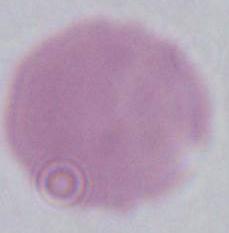
magnification = 1000x
modality = micrograph
identification = red blood cell